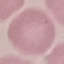 Result: negative for malaria parasites. Thin blood smear. Giemsa-stained preparation. Automatically extracted cell patch, resized to 64 × 64 pixels. Photographed with a smartphone camera at the microscope eyepiece.